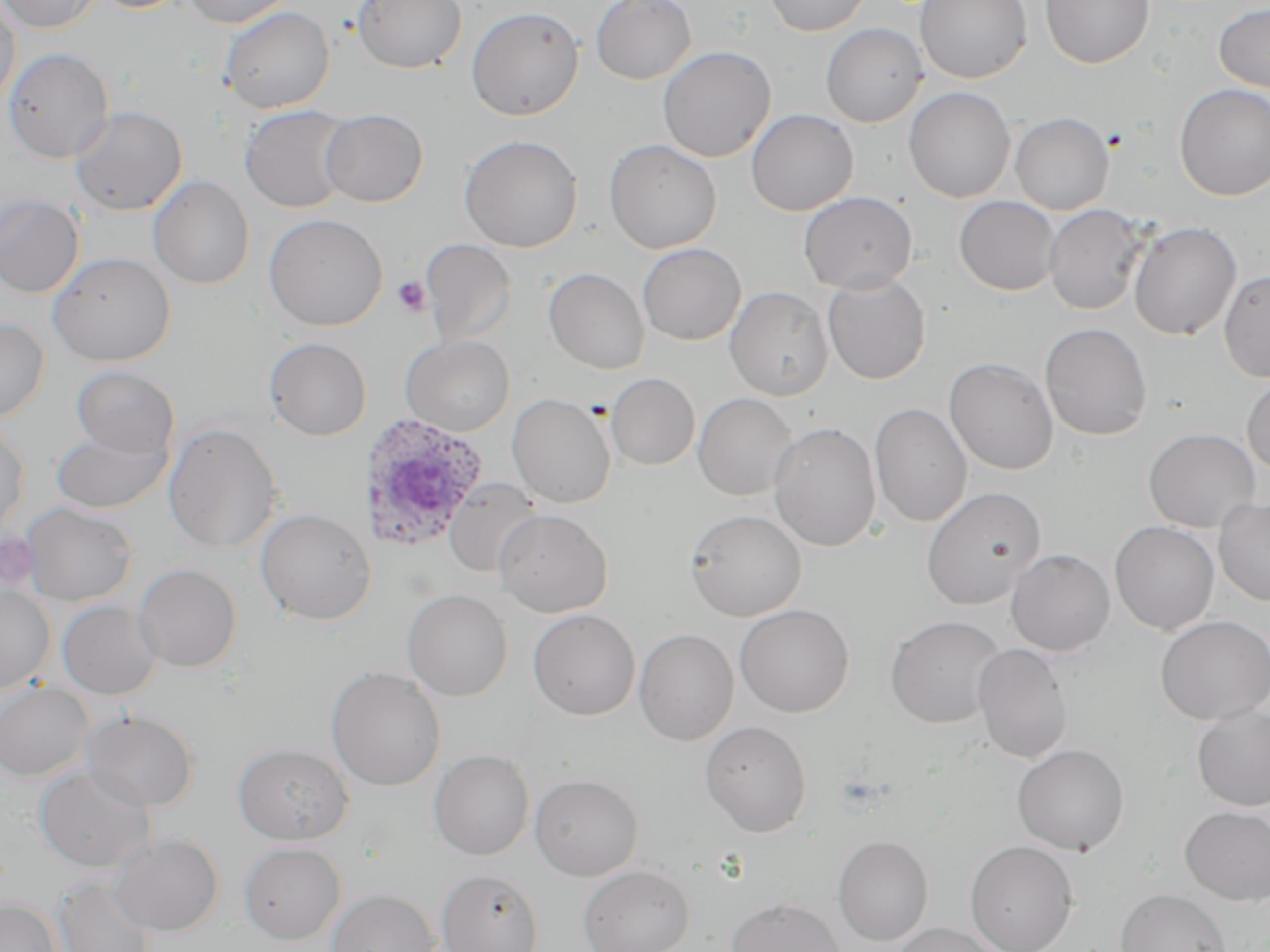 Approximate bounding boxes as named x1/y1/x2/y2 corners in pixels. Uninfected red blood cell locations: (x1=0, y1=0, x2=21, y2=109), (x1=2, y1=0, x2=100, y2=34), (x1=90, y1=0, x2=192, y2=13), (x1=182, y1=0, x2=295, y2=28), (x1=352, y1=0, x2=467, y2=74), (x1=590, y1=0, x2=696, y2=85), (x1=764, y1=0, x2=872, y2=36), (x1=914, y1=0, x2=1032, y2=83), (x1=1040, y1=0, x2=1154, y2=68), (x1=1213, y1=4, x2=1270, y2=94), (x1=220, y1=6, x2=335, y2=114), (x1=466, y1=6, x2=584, y2=121), (x1=820, y1=23, x2=927, y2=128), (x1=658, y1=46, x2=776, y2=163), (x1=3, y1=47, x2=114, y2=163), (x1=1174, y1=83, x2=1270, y2=200), (x1=904, y1=87, x2=1016, y2=203), (x1=70, y1=105, x2=188, y2=216), (x1=239, y1=105, x2=353, y2=213), (x1=320, y1=108, x2=428, y2=207), (x1=746, y1=109, x2=858, y2=216), (x1=1009, y1=112, x2=1114, y2=214), (x1=459, y1=135, x2=583, y2=252), (x1=603, y1=139, x2=722, y2=254), (x1=148, y1=175, x2=255, y2=290), (x1=798, y1=191, x2=917, y2=294), (x1=0, y1=194, x2=84, y2=297), (x1=954, y1=196, x2=1061, y2=296), (x1=1043, y1=204, x2=1148, y2=315), (x1=264, y1=213, x2=388, y2=331), (x1=1128, y1=222, x2=1242, y2=340), (x1=420, y1=239, x2=517, y2=347), (x1=637, y1=243, x2=746, y2=346), (x1=48, y1=252, x2=176, y2=366), (x1=543, y1=268, x2=650, y2=374), (x1=1219, y1=270, x2=1270, y2=383), (x1=822, y1=273, x2=930, y2=384), (x1=724, y1=286, x2=834, y2=401), (x1=0, y1=318, x2=49, y2=421), (x1=1039, y1=322, x2=1153, y2=441), (x1=401, y1=335, x2=515, y2=436), (x1=264, y1=337, x2=372, y2=441), (x1=943, y1=358, x2=1058, y2=475), (x1=71, y1=367, x2=179, y2=458), (x1=606, y1=373, x2=700, y2=470), (x1=1242, y1=375, x2=1270, y2=475), (x1=693, y1=392, x2=798, y2=501), (x1=507, y1=393, x2=616, y2=508), (x1=869, y1=403, x2=971, y2=527), (x1=0, y1=421, x2=30, y2=535), (x1=162, y1=422, x2=283, y2=554), (x1=767, y1=422, x2=881, y2=552), (x1=50, y1=424, x2=173, y2=514), (x1=1144, y1=428, x2=1261, y2=533), (x1=444, y1=479, x2=541, y2=577), (x1=921, y1=486, x2=1045, y2=610), (x1=1213, y1=497, x2=1270, y2=607), (x1=22, y1=502, x2=139, y2=607), (x1=255, y1=508, x2=376, y2=625), (x1=494, y1=509, x2=613, y2=617), (x1=685, y1=509, x2=806, y2=622), (x1=1109, y1=521, x2=1219, y2=635), (x1=1005, y1=549, x2=1115, y2=656), (x1=133, y1=563, x2=242, y2=672), (x1=0, y1=585, x2=55, y2=695), (x1=401, y1=589, x2=512, y2=702), (x1=57, y1=600, x2=163, y2=700), (x1=734, y1=604, x2=854, y2=717), (x1=528, y1=609, x2=640, y2=720), (x1=885, y1=615, x2=1006, y2=729), (x1=1154, y1=615, x2=1270, y2=725), (x1=633, y1=628, x2=739, y2=745), (x1=972, y1=643, x2=1072, y2=763), (x1=326, y1=666, x2=446, y2=791), (x1=0, y1=682, x2=93, y2=782), (x1=1192, y1=703, x2=1270, y2=811), (x1=81, y1=709, x2=199, y2=811), (x1=700, y1=721, x2=812, y2=836), (x1=233, y1=743, x2=353, y2=845), (x1=1012, y1=743, x2=1130, y2=856), (x1=428, y1=749, x2=534, y2=861), (x1=34, y1=765, x2=156, y2=873), (x1=529, y1=773, x2=644, y2=880), (x1=1179, y1=806, x2=1270, y2=905), (x1=109, y1=833, x2=224, y2=936), (x1=832, y1=835, x2=933, y2=946), (x1=965, y1=840, x2=1079, y2=952), (x1=239, y1=842, x2=346, y2=944), (x1=577, y1=863, x2=694, y2=952), (x1=436, y1=868, x2=545, y2=952), (x1=52, y1=875, x2=155, y2=952), (x1=327, y1=888, x2=440, y2=952), (x1=1116, y1=888, x2=1231, y2=952), (x1=727, y1=897, x2=845, y2=952), (x1=0, y1=898, x2=60, y2=952), (x1=890, y1=923, x2=1007, y2=951). Platelet locations: (x1=392, y1=276, x2=431, y2=316). Plasmodium ovale-infected red blood cell locations: (x1=359, y1=412, x2=488, y2=553). Slide-level diagnosis: Plasmodium ovale. Single field of view. Thin blood film. Optical microscopy. Captured at 1000x magnification. May-Grünwald-Giemsa-stained preparation. Image is 1270×952 pixels.